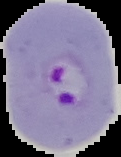

image size = 121×157 pixels
image type = segmented cell region on a black background
malaria status = parasitized
preparation = thin blood smear